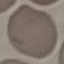
malaria_status: uninfected
capture: smartphone through the microscope eyepiece
image_type: automatically extracted cell patch, resized to 64 × 64 pixels
stain: Giemsa
preparation: thin blood film